Locate and identify every blood parasite.
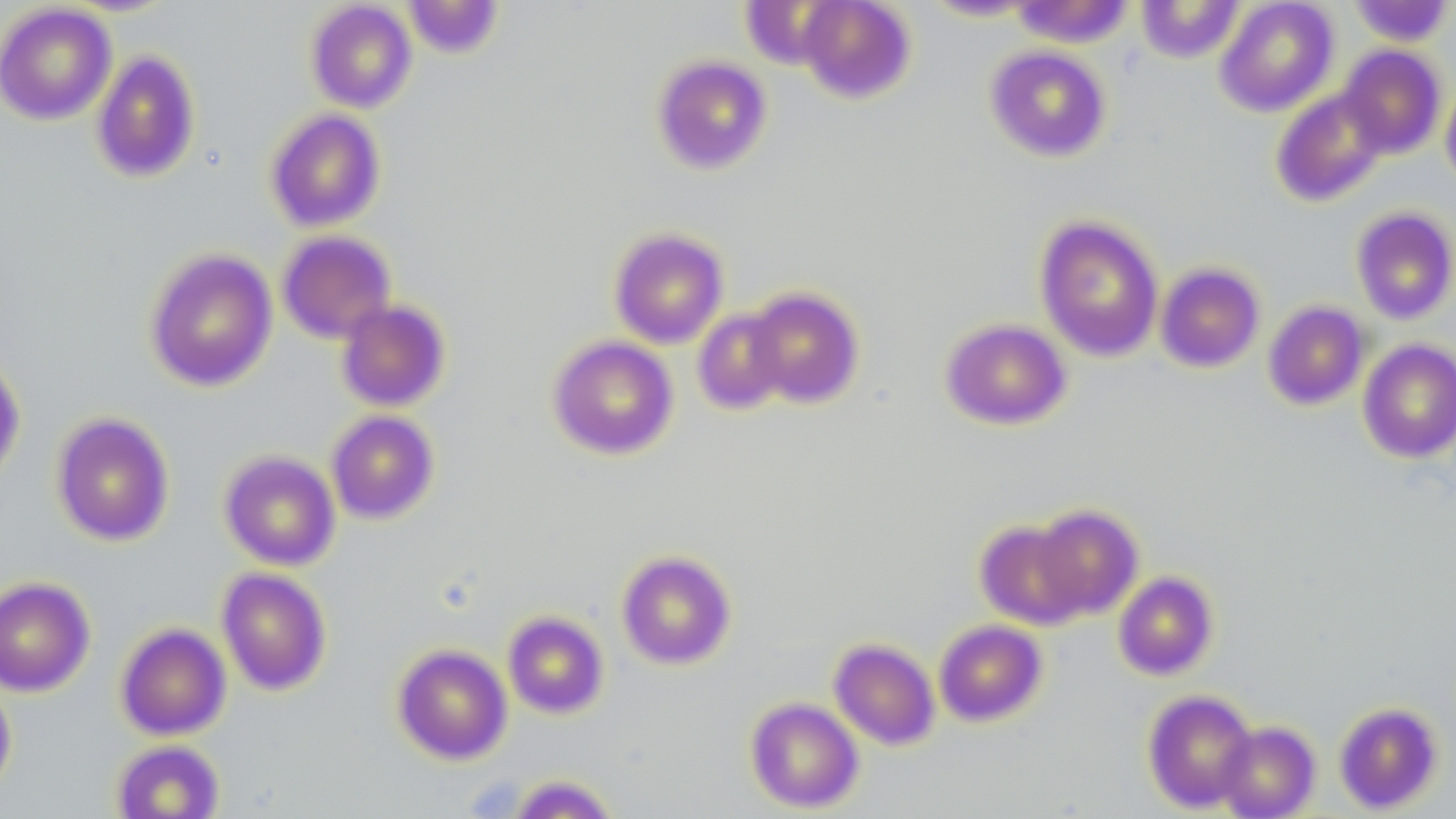
No blood parasites seen.

slide-level diagnosis = no evidence of blood parasites
modality = optical microscopy
preparation = thin blood smear
field of view = single
image size = 1456×819 pixels
stain = May-Grünwald-Giemsa
uninfected red blood cell locations = approximate bounding boxes as named x1/y1/x2/y2 corners in pixels: (x1=402, y1=0, x2=504, y2=59), (x1=797, y1=0, x2=916, y2=103), (x1=1136, y1=0, x2=1244, y2=63), (x1=1214, y1=0, x2=1339, y2=117), (x1=305, y1=1, x2=417, y2=113), (x1=919, y1=1, x2=1045, y2=22), (x1=1010, y1=1, x2=1134, y2=47), (x1=1348, y1=1, x2=1454, y2=46), (x1=0, y1=3, x2=117, y2=125), (x1=1337, y1=44, x2=1446, y2=159), (x1=985, y1=45, x2=1112, y2=162), (x1=90, y1=49, x2=201, y2=183), (x1=652, y1=54, x2=772, y2=174), (x1=1440, y1=77, x2=1456, y2=189), (x1=1271, y1=87, x2=1389, y2=206), (x1=265, y1=108, x2=386, y2=232), (x1=1351, y1=206, x2=1456, y2=325), (x1=1034, y1=215, x2=1164, y2=362), (x1=609, y1=227, x2=729, y2=348), (x1=276, y1=230, x2=397, y2=344), (x1=144, y1=248, x2=278, y2=392), (x1=1154, y1=262, x2=1265, y2=373), (x1=745, y1=287, x2=864, y2=409), (x1=335, y1=298, x2=451, y2=412), (x1=1263, y1=300, x2=1369, y2=411), (x1=691, y1=307, x2=791, y2=415), (x1=940, y1=318, x2=1070, y2=430), (x1=548, y1=334, x2=679, y2=460), (x1=1358, y1=338, x2=1456, y2=463), (x1=0, y1=349, x2=26, y2=486), (x1=326, y1=410, x2=439, y2=524), (x1=51, y1=411, x2=174, y2=547), (x1=218, y1=449, x2=341, y2=570), (x1=1031, y1=504, x2=1144, y2=620), (x1=975, y1=519, x2=1088, y2=630), (x1=617, y1=550, x2=736, y2=669), (x1=217, y1=567, x2=332, y2=696), (x1=1113, y1=570, x2=1218, y2=680), (x1=0, y1=575, x2=96, y2=697), (x1=502, y1=611, x2=608, y2=719), (x1=933, y1=619, x2=1047, y2=726), (x1=115, y1=622, x2=232, y2=741), (x1=828, y1=638, x2=940, y2=750), (x1=393, y1=643, x2=512, y2=764), (x1=0, y1=675, x2=17, y2=799), (x1=1142, y1=688, x2=1258, y2=813), (x1=745, y1=696, x2=864, y2=813), (x1=1334, y1=701, x2=1443, y2=814), (x1=1216, y1=721, x2=1320, y2=818), (x1=111, y1=739, x2=225, y2=819), (x1=506, y1=774, x2=621, y2=818)
magnification = 1000x